Report the malaria status of this cell.
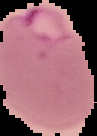
It is parasitized.

Summary:
  - Image type: segmented cell region on a black background
  - Image size: 97×136 pixels
  - Preparation: thin blood film